State the blood parasite species.
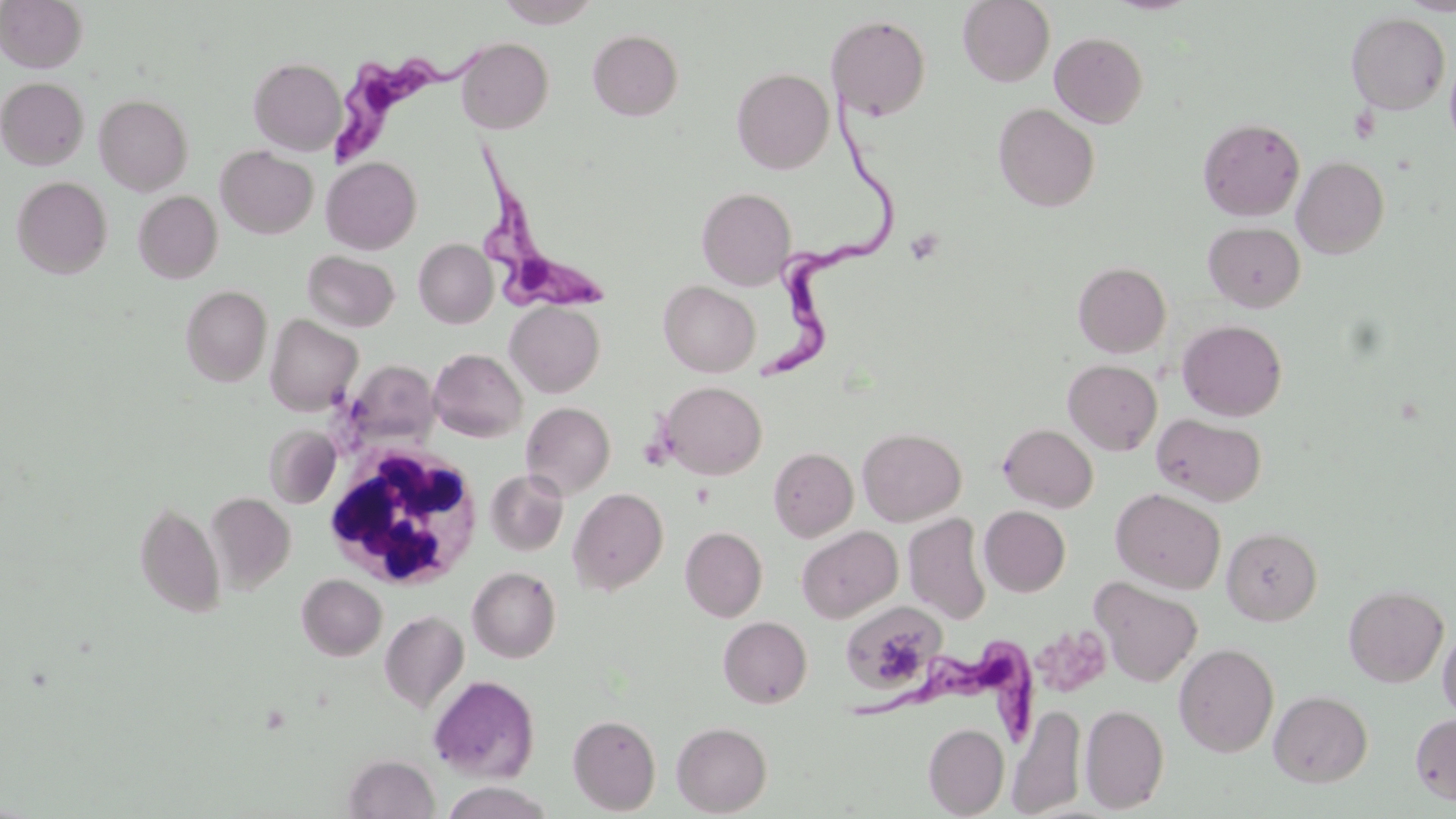

Trypanosoma brucei.

field of view = one of a larger specimen
platelet locations = approximate bounding boxes as [x1, y1, x2, y2] in pixels: [905, 228, 944, 265], [1040, 627, 1109, 694]
stain = May-Grünwald-Giemsa
magnification = 1000x
preparation = thin blood film
image size = 1456×819 pixels
modality = light microscopy
Trypanosoma brucei locations = approximate bounding boxes as [x1, y1, x2, y2] in pixels: [328, 43, 487, 168], [744, 80, 896, 383], [471, 140, 603, 318], [853, 645, 1036, 742]
uninfected red blood cell locations = approximate bounding boxes as [x1, y1, x2, y2] in pixels: [0, 0, 87, 72], [496, 0, 601, 27], [958, 0, 1055, 86], [1400, 0, 1456, 15], [1346, 12, 1450, 114], [827, 15, 931, 120], [587, 29, 683, 120], [1050, 31, 1148, 128], [455, 37, 553, 133], [1445, 53, 1456, 152], [249, 58, 345, 155], [732, 67, 834, 174], [0, 77, 88, 169], [94, 94, 193, 194], [993, 103, 1100, 212], [1198, 117, 1305, 221], [216, 145, 318, 239], [321, 156, 422, 254], [1292, 156, 1390, 259], [11, 176, 112, 278], [697, 187, 796, 290], [133, 191, 222, 282], [1203, 222, 1306, 313], [414, 238, 497, 328], [302, 251, 400, 332], [1073, 261, 1171, 357], [659, 280, 760, 376], [181, 285, 272, 386], [505, 301, 605, 397], [265, 314, 363, 415], [1177, 319, 1288, 421], [429, 348, 527, 443], [344, 359, 440, 449], [1063, 359, 1162, 455], [660, 381, 766, 479], [521, 401, 616, 499], [1152, 413, 1266, 506], [998, 423, 1098, 512], [264, 425, 340, 508], [857, 427, 966, 526], [768, 447, 858, 541], [485, 469, 569, 556], [1111, 487, 1226, 594], [568, 488, 668, 595], [206, 493, 295, 591], [133, 501, 225, 618], [979, 505, 1070, 597], [903, 513, 992, 624], [796, 525, 902, 623], [681, 526, 767, 622], [1222, 527, 1322, 625], [468, 566, 561, 662], [297, 574, 387, 660], [1090, 577, 1203, 687], [1343, 584, 1449, 687], [840, 602, 946, 695], [379, 611, 469, 713], [718, 616, 812, 707], [1438, 626, 1456, 722], [1174, 643, 1279, 757], [429, 675, 540, 782], [1269, 690, 1373, 787], [1007, 703, 1086, 818], [1080, 704, 1169, 813], [1410, 712, 1456, 807], [568, 713, 661, 814], [672, 721, 772, 816], [924, 723, 1009, 817], [343, 753, 439, 818], [438, 781, 556, 819]
white blood cell locations = approximate bounding boxes as [x1, y1, x2, y2] in pixels: [323, 441, 484, 590]